Classify this cell by malaria status.
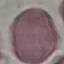

Uninfected.

Acquired by smartphone through the microscope eyepiece. Automatically extracted cell patch, resized to 64 × 64 pixels. Giemsa stain. Thin blood smear.